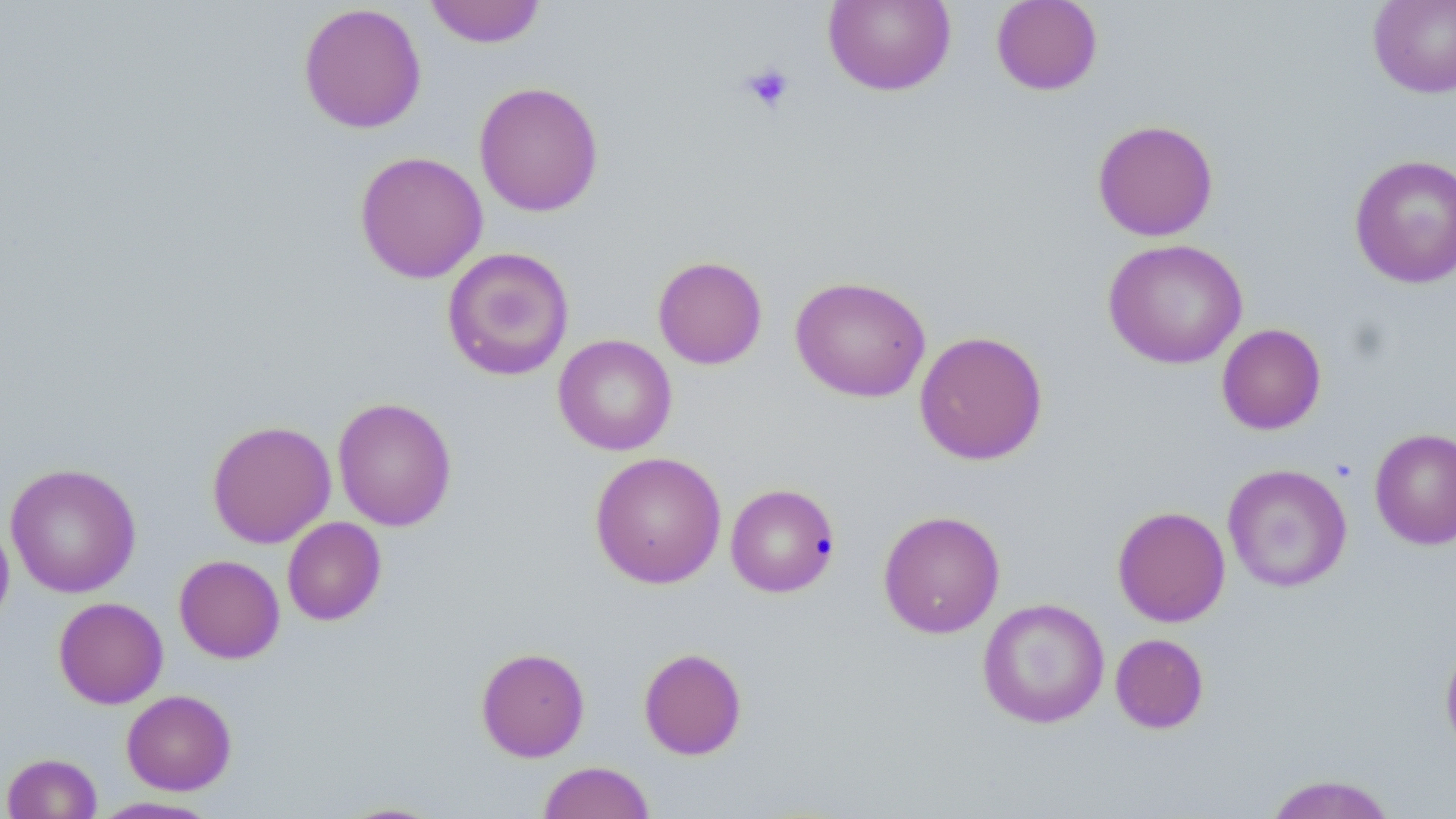

slide_level_diagnosis: no evidence of blood parasites
stain: May-Grünwald-Giemsa
uninfected_red_blood_cell_locations: 'approximate bounding boxes as (x1, y1, x2, y2) in pixels: (424, 0, 546, 48), (823, 0, 956, 96), (991, 0, 1103, 95), (1368, 0, 1456, 98), (298, 3, 427, 134), (474, 81, 604, 217), (1092, 119, 1219, 241), (354, 151, 488, 283), (1349, 154, 1456, 289), (1103, 239, 1247, 369), (441, 246, 575, 381), (652, 256, 767, 370), (790, 275, 930, 402), (1216, 323, 1326, 435), (914, 330, 1048, 466), (553, 334, 677, 456), (332, 397, 457, 531), (207, 420, 336, 548), (1370, 427, 1456, 550), (589, 451, 727, 589), (4, 463, 142, 598), (1222, 463, 1352, 593), (725, 483, 840, 597), (1112, 505, 1231, 627), (878, 510, 1005, 639), (0, 515, 14, 628), (282, 517, 386, 626), (174, 555, 285, 664), (53, 597, 168, 708), (977, 598, 1110, 729), (1110, 633, 1209, 734), (1439, 636, 1456, 760), (476, 647, 590, 762), (639, 647, 747, 760), (121, 689, 236, 795), (2, 752, 103, 819), (537, 761, 654, 819), (1262, 774, 1399, 818), (90, 796, 224, 818), (332, 800, 448, 818)'
magnification: 1000x
image_size: 1456×819 pixels
modality: optical microscopy
platelet_locations: 'approximate bounding boxes as (x1, y1, x2, y2) in pixels: (740, 63, 794, 114)'
field_of_view: single
preparation: thin blood smear